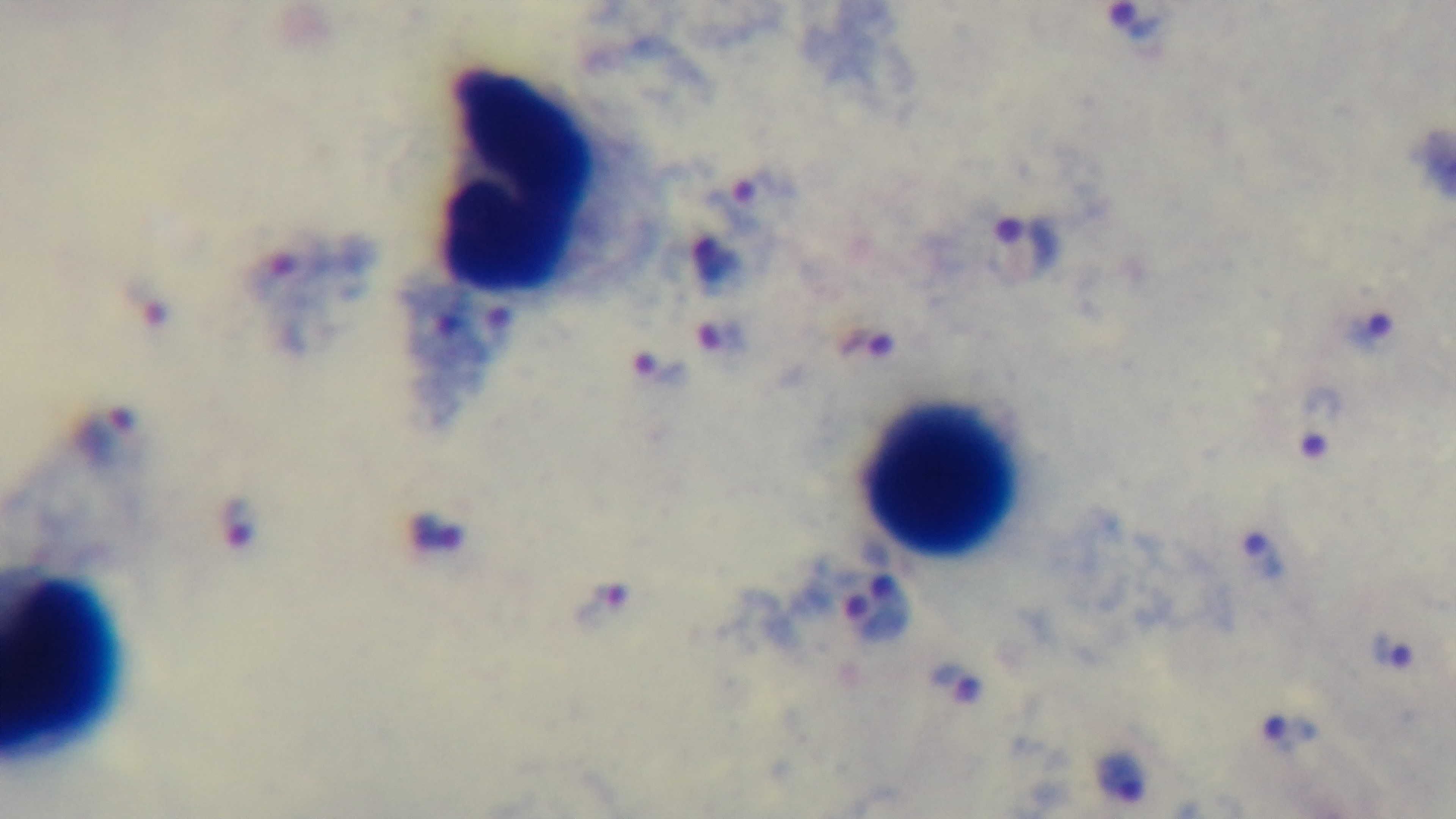
modality = light microscopy
preparation = thick smear
capture = mounted 4K digital camera
stain = Giemsa
objective = 100x oil immersion
field of view = one from the slide
malaria status = positive